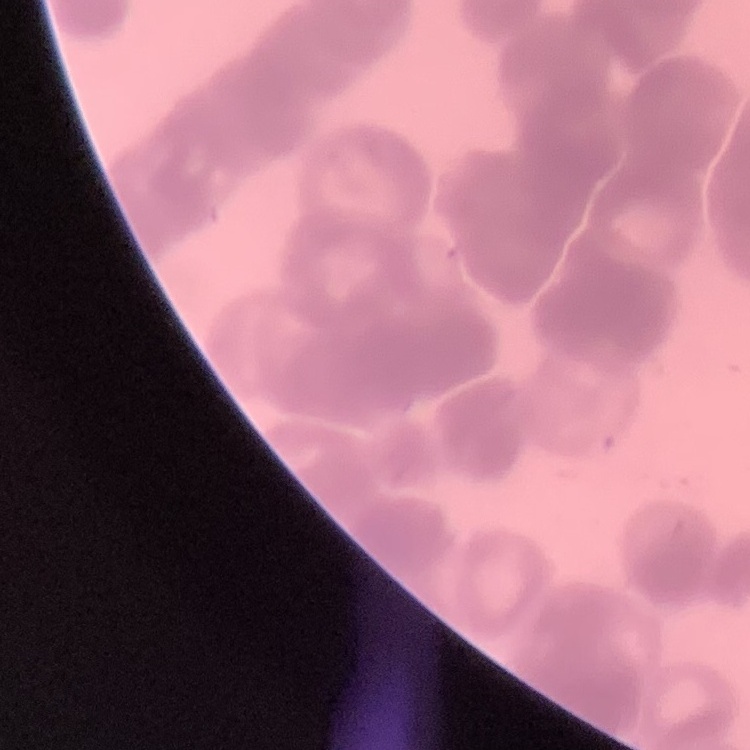

Summary:
  - Red blood cell morphology: rouleaux formation
  - Image type: one tile cut from a larger photomicrograph
  - Stain: Field's or Giemsa
  - Preparation: thin peripheral smear